Comment on the morphology of the erythrocytes.
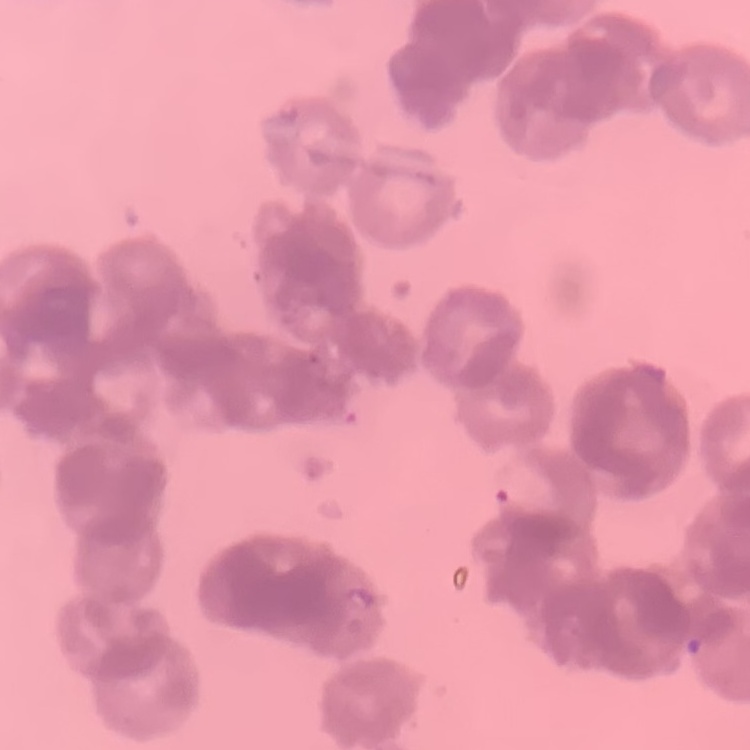

They show rouleaux formation.

Square crop of a larger photomicrograph. Thin blood smear. Stained with either Field's or Giemsa.